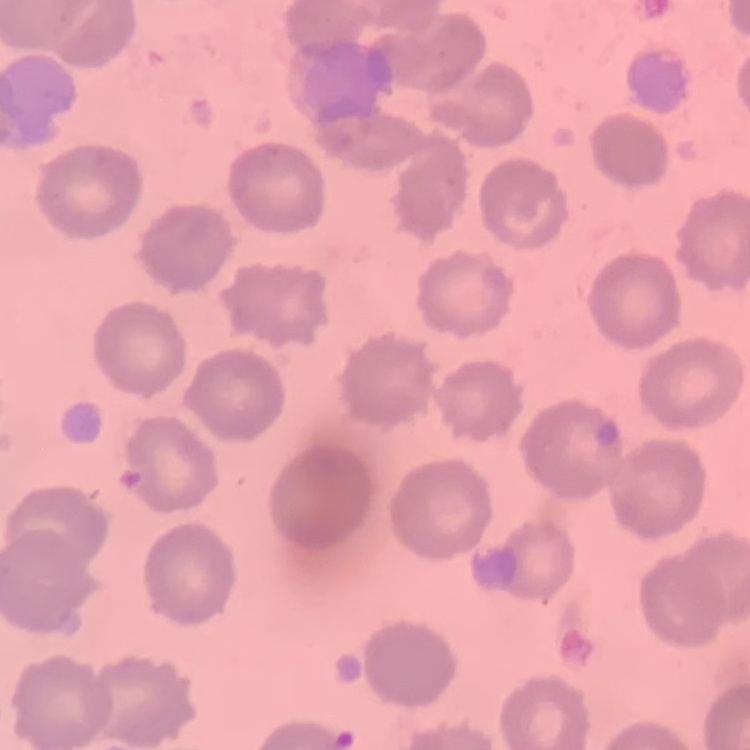
The red blood cells show no rouleaux formation. Square crop of a larger photomicrograph. Stained with either Field's or Giemsa. Thin blood film.